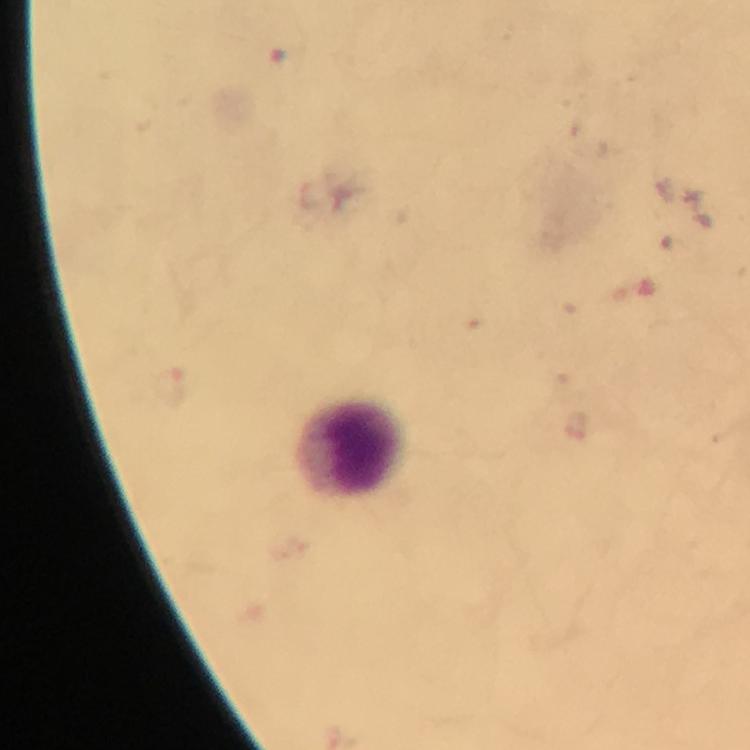

immersion oil = applied
image size = 750×750 pixels
Plasmodium parasites = none detected
context = from a diagnostic examination for malaria
magnification = 100x
capture = smartphone camera through the microscope
cropped from = one field of view
leukocyte locations = approximate centers as [x, y] in pixels: [350, 449]
stain = Giemsa
preparation = thick blood smear